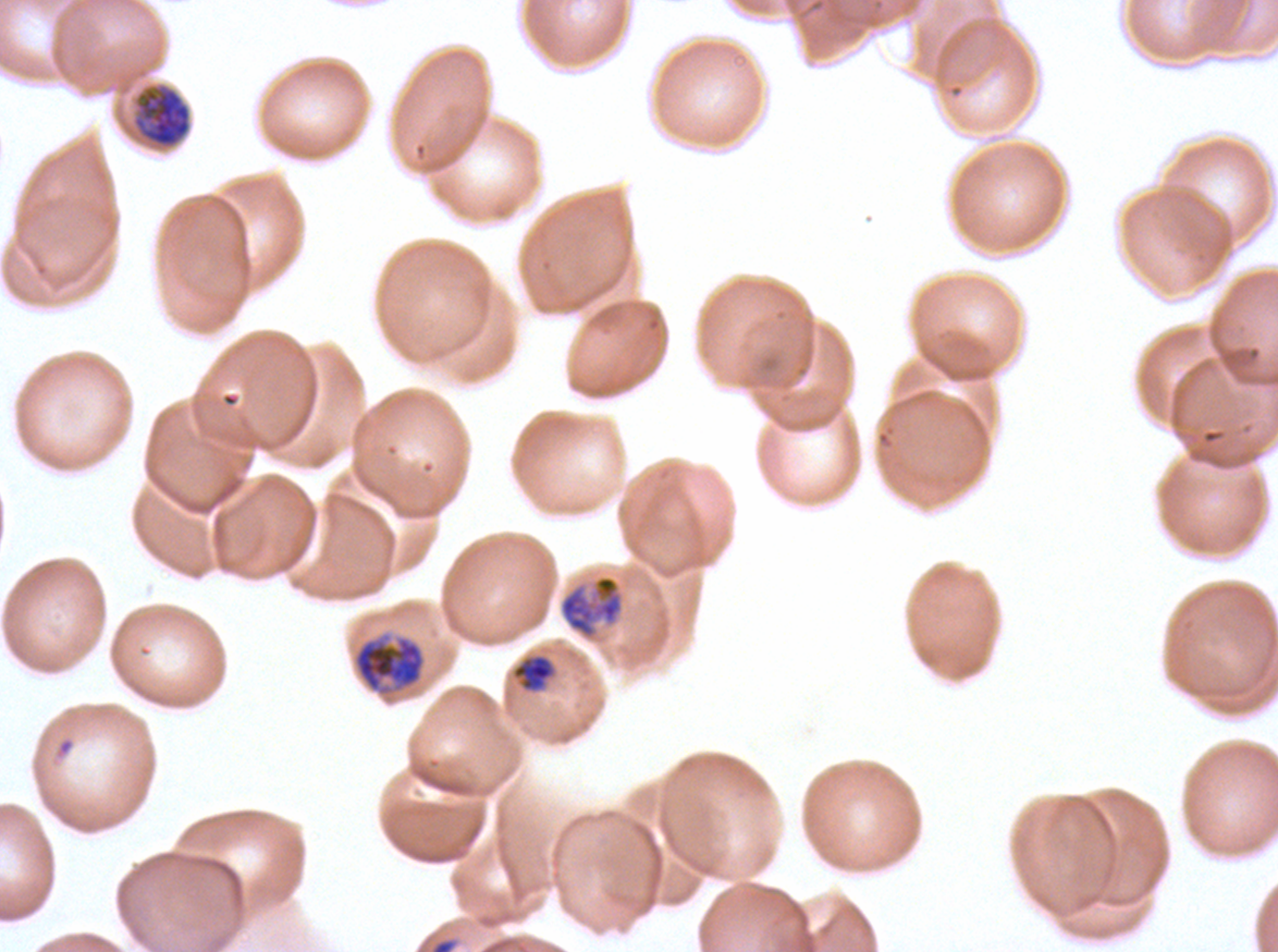
Approximate bounding rectangles given as corner coordinates in pixels from the top-left.
Summary:
  - Debris locations: (x1=428, y1=936, x2=460, y2=951)
  - Late-ring/early-trophozoite locations: (x1=511, y1=653, x2=556, y2=692)
  - Early schizont locations: (x1=132, y1=84, x2=191, y2=149), (x1=352, y1=635, x2=425, y2=696)
  - Late trophozoite locations: (x1=559, y1=574, x2=624, y2=640)
  - Stain: Giemsa
  - Specimen: ex-vivo Plasmodium falciparum culture from a patient in The Gambia, grown for 24 to 48 hours
  - Image size: 1278×952 pixels
  - Field of view: one sub-image of a larger composite
  - Life-cycle stages observed: late-ring/early-trophozoite, late trophozoite, early schizont
  - Preparation: thin blood smear